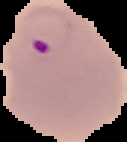

Summary:
  - Malaria status: parasitized
  - Image size: 127×142 pixels
  - Image type: segmented cell region on a black background
  - Preparation: thin blood smear